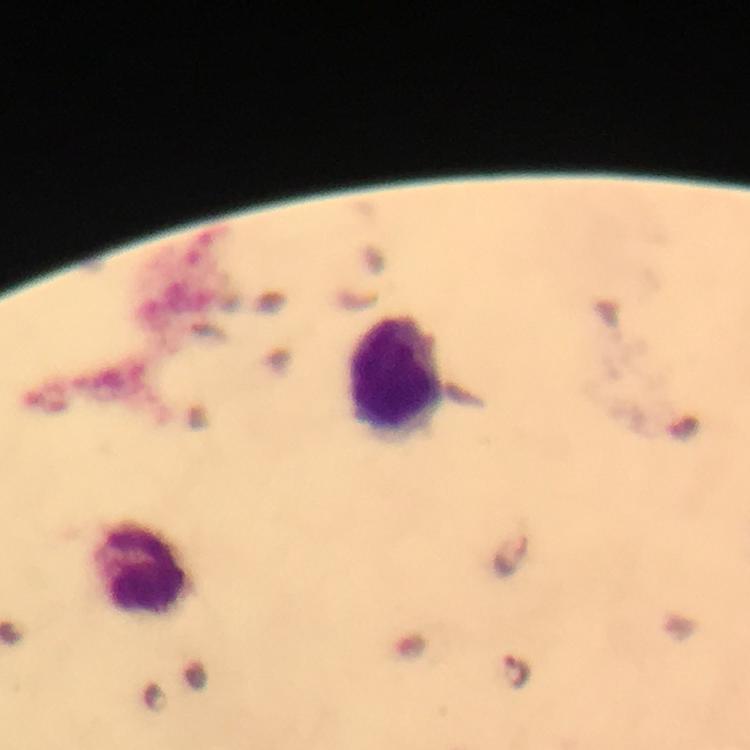
Approximate object centers, in pixels from the top-left corner.
Summary:
  - Leukocyte locations: (x=396, y=382), (x=140, y=571)
  - Malaria parasite locations: (x=517, y=671)
  - Cropped from: a single field of view
  - Image size: 750×750 pixels
  - Magnification: 100x
  - Stain: Giemsa
  - Capture: smartphone photograph through a microscope
  - Context: from a diagnostic examination for malaria
  - Preparation: thick smear
  - Immersion oil: applied